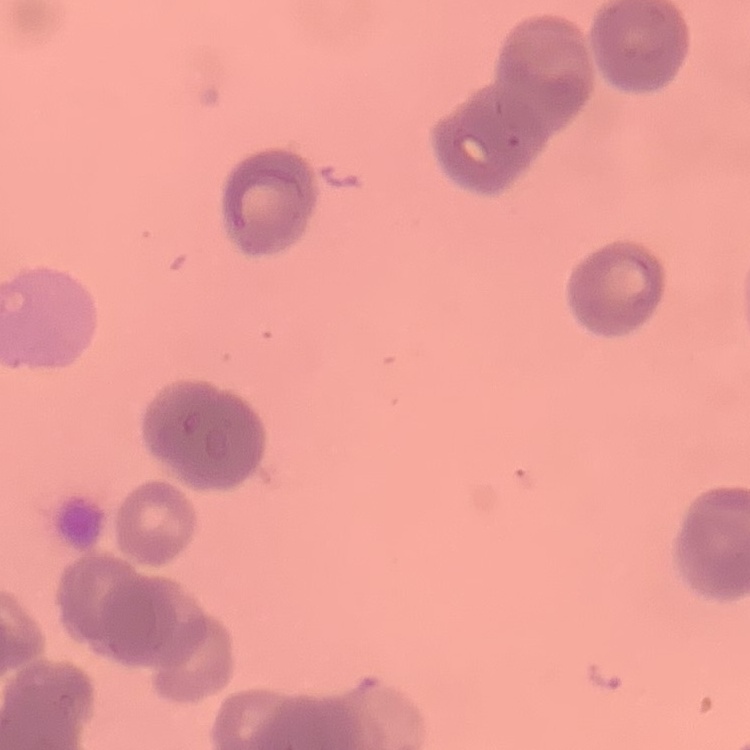 The erythrocytes show rouleaux formation. Stained with either Field's or Giemsa. Thin peripheral smear. One tile cut from a larger photomicrograph.